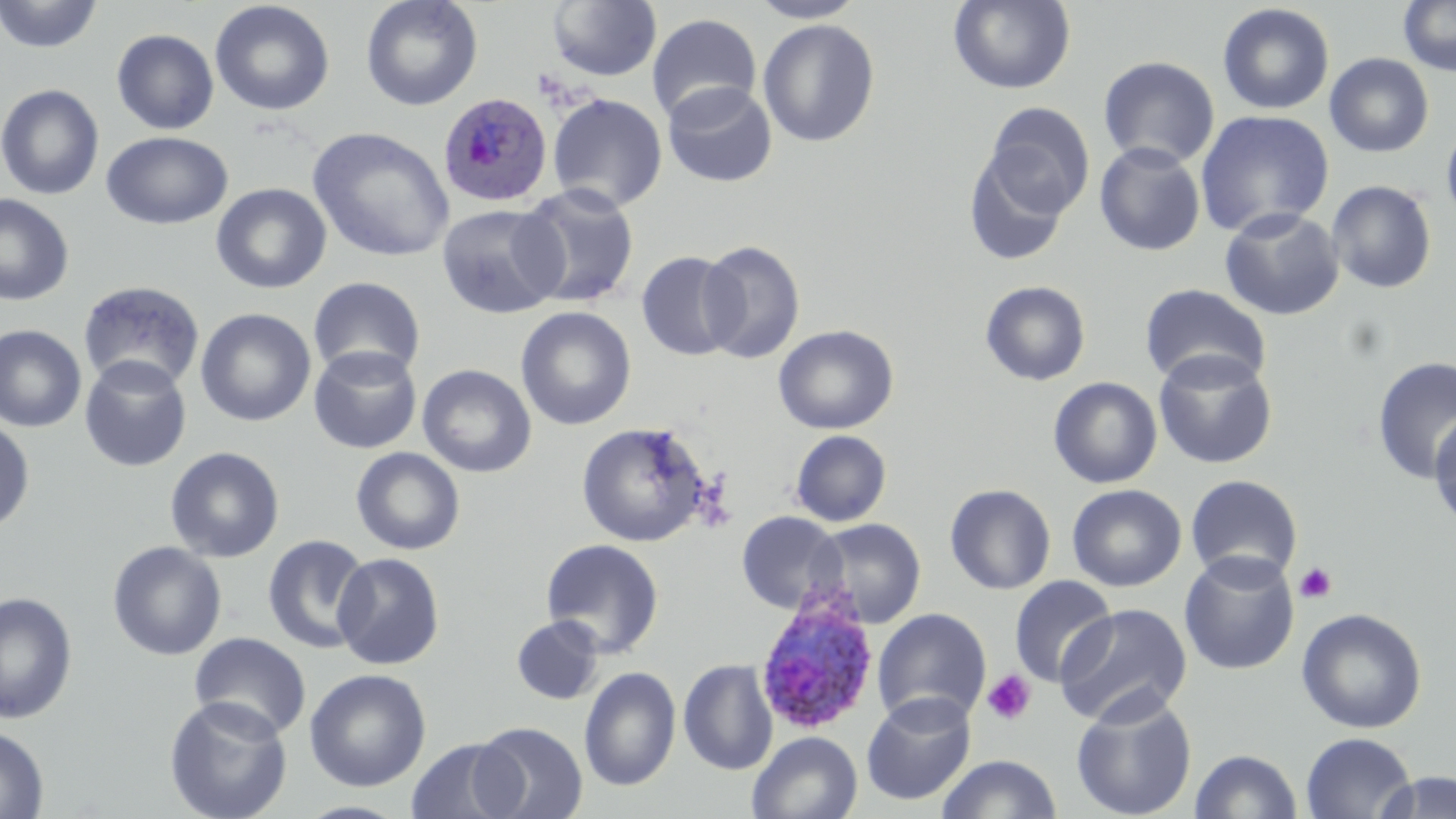
{
  "slide_level_diagnosis": "Plasmodium ovale",
  "platelet_locations": "approximate bounding boxes as (x1, y1, x2, y2) in pixels: (1293, 562, 1338, 604), (981, 669, 1037, 726)",
  "modality": "light microscopy",
  "stain": "May-Grünwald-Giemsa",
  "uninfected_red_blood_cell_locations": "approximate bounding boxes as (x1, y1, x2, y2) in pixels: (0, 0, 102, 54), (361, 0, 483, 111), (748, 0, 867, 23), (948, 0, 1076, 94), (1398, 0, 1456, 76), (210, 1, 335, 117), (546, 1, 662, 82), (1217, 3, 1335, 115), (646, 12, 762, 123), (757, 19, 880, 147), (111, 29, 219, 134), (1324, 52, 1434, 158), (1098, 56, 1220, 169), (662, 81, 777, 187), (0, 84, 104, 200), (547, 93, 668, 212), (982, 102, 1094, 220), (1195, 109, 1335, 237), (1440, 119, 1456, 230), (307, 127, 455, 263), (101, 131, 232, 230), (1094, 141, 1206, 256), (963, 146, 1075, 266), (1326, 179, 1438, 294), (210, 182, 332, 294), (515, 183, 640, 309), (0, 193, 74, 306), (437, 203, 567, 319), (1219, 207, 1345, 321), (697, 240, 805, 363), (636, 251, 742, 362), (308, 276, 426, 382), (77, 280, 205, 393), (980, 280, 1091, 386), (1140, 283, 1272, 390), (516, 306, 636, 430), (195, 307, 316, 427), (773, 324, 898, 434), (0, 325, 86, 433), (308, 345, 422, 454), (1153, 350, 1278, 469), (79, 355, 192, 472), (1370, 356, 1456, 484), (417, 364, 537, 477), (1048, 376, 1162, 489), (1429, 408, 1456, 532), (0, 418, 35, 534), (575, 421, 711, 547), (790, 430, 891, 526), (165, 446, 285, 563), (351, 447, 465, 555), (1185, 474, 1303, 584), (944, 484, 1056, 595), (1067, 484, 1187, 591), (735, 511, 846, 614), (808, 518, 926, 629), (262, 534, 373, 654), (541, 538, 664, 658), (107, 541, 227, 661), (1179, 551, 1300, 675), (332, 552, 445, 670), (1008, 575, 1117, 689), (0, 591, 78, 725), (1055, 604, 1193, 727), (1296, 607, 1428, 733), (872, 608, 991, 728), (511, 615, 604, 705), (189, 632, 312, 740), (678, 659, 778, 776), (579, 666, 681, 792), (304, 668, 431, 792), (1070, 692, 1198, 819), (861, 693, 976, 806), (164, 696, 293, 819), (471, 722, 588, 819), (0, 726, 49, 818), (747, 731, 862, 819), (1300, 731, 1417, 819), (407, 737, 522, 819), (1189, 749, 1302, 818), (934, 754, 1063, 818), (1369, 770, 1456, 818), (295, 800, 412, 819)",
  "image_size": "1456×819 pixels",
  "preparation": "thin blood film",
  "magnification": "1000x",
  "plasmodium_ovale_infected_red_blood_cell_locations": "approximate bounding boxes as (x1, y1, x2, y2) in pixels: (438, 93, 552, 207), (754, 593, 880, 735)",
  "field_of_view": "single"
}